Report the malaria status of this cell.
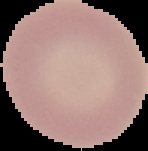

Uninfected.

Summary:
  - Image type: cell region segmented out of the field of view; surrounding area masked to black
  - Preparation: thin blood film
  - Image size: 148×151 pixels